Classify this cell by malaria status.
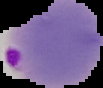

It is parasitized.

image size = 103×88 pixels
image type = cell region segmented out of the field of view; surrounding area masked to black
preparation = thin blood film